Assess this cell for malaria.
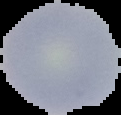
It is uninfected.

Summary:
  - Preparation: thin blood film
  - Image type: segmented cell region on a black background
  - Image size: 121×115 pixels